Identify the parasite.
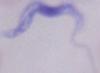

This is a trypanosome.

magnification = 1000x
modality = micrograph